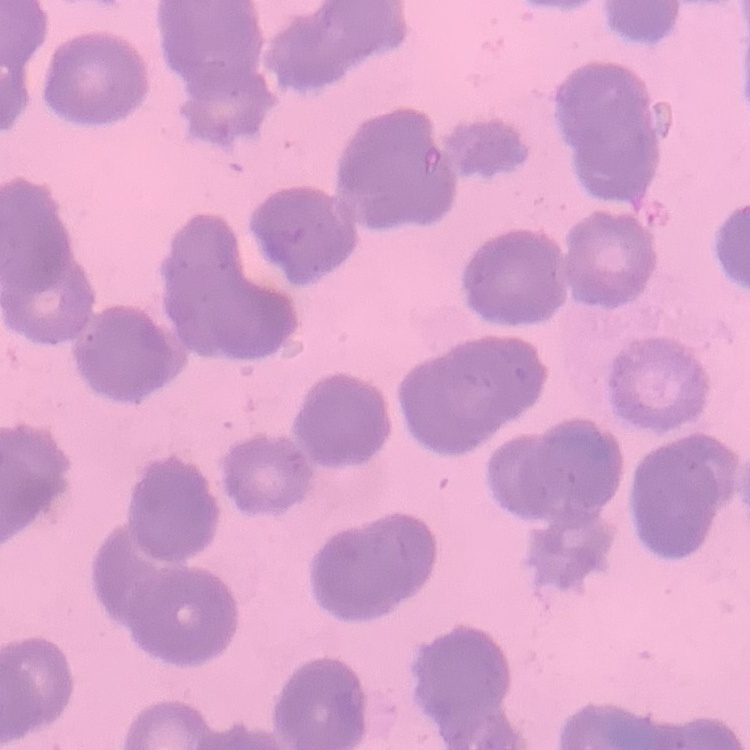

erythrocyte morphology = rouleaux formation
image type = square crop of a larger photomicrograph
stain = Field's or Giemsa
preparation = thin blood film